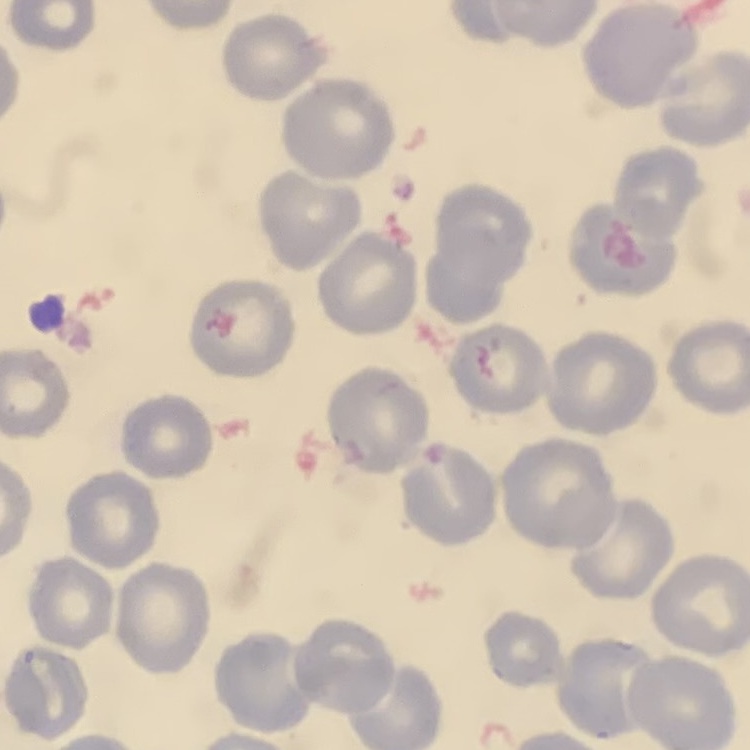

erythrocyte morphology = no rouleaux formation
stain = Field's or Giemsa
image type = square crop of a larger photomicrograph
preparation = thin blood film